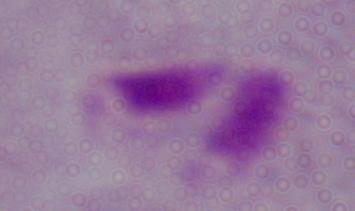 Photomicrograph. A trichomonad is shown. Captured at 1000x magnification.